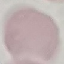
Summary:
  - Result: no malaria parasites seen
  - Preparation: thin blood smear
  - Capture: smartphone camera at the microscope eyepiece
  - Stain: Giemsa
  - Image type: cell patch, automatically extracted from a larger field of view and resized to 64 × 64 pixels